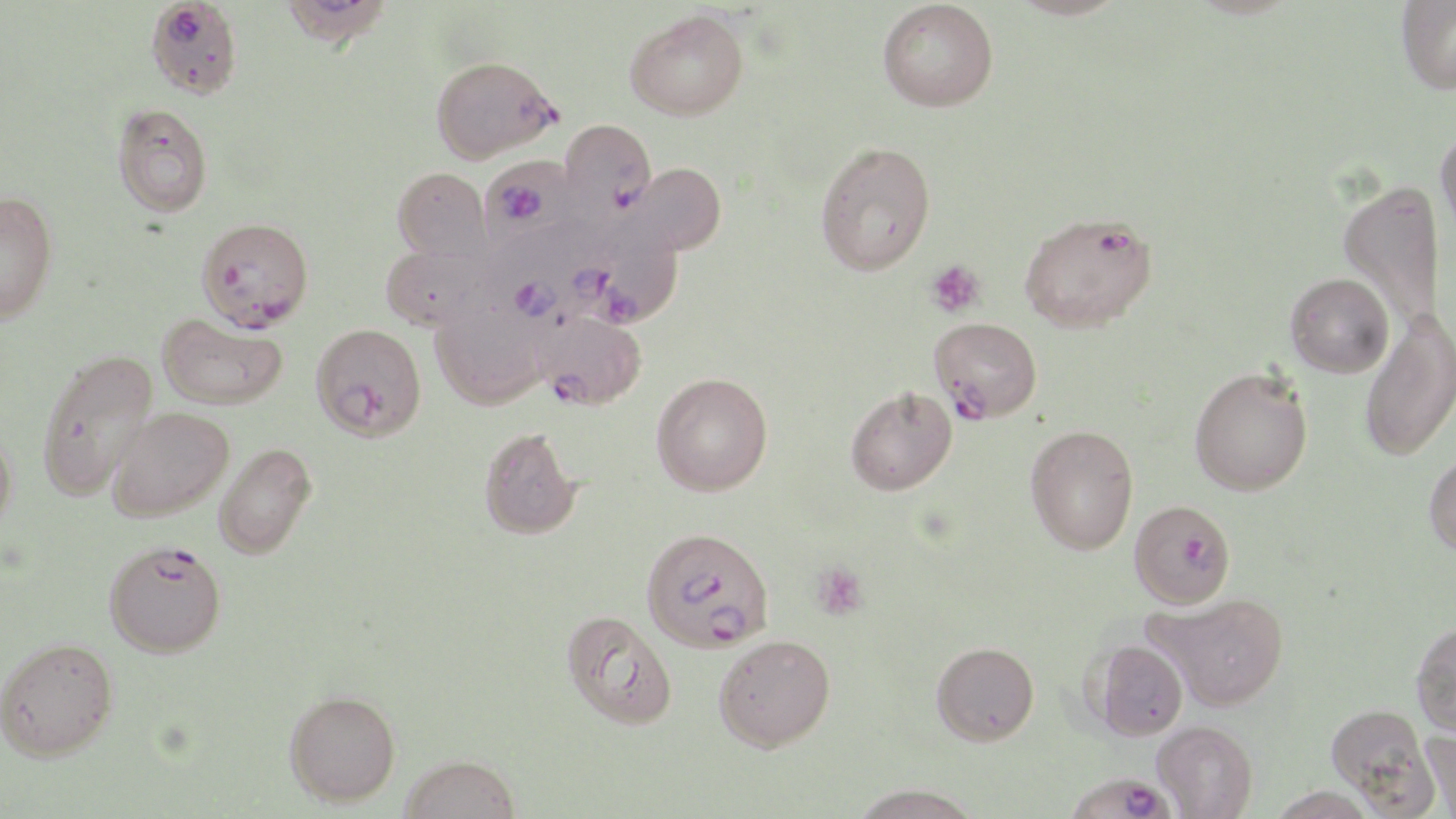

Summary:
  - Coordinate format: approximate bounding boxes as named x1/y1/x2/y2 corners in pixels
  - Plasmodium falciparum-infected red blood cell locations (subset): (x1=278, y1=0, x2=392, y2=49), (x1=430, y1=55, x2=560, y2=163), (x1=559, y1=118, x2=657, y2=221), (x1=479, y1=156, x2=584, y2=243), (x1=1019, y1=210, x2=1158, y2=333), (x1=196, y1=216, x2=313, y2=330), (x1=580, y1=216, x2=684, y2=328), (x1=485, y1=231, x2=602, y2=340), (x1=535, y1=310, x2=647, y2=410), (x1=929, y1=316, x2=1042, y2=422), (x1=311, y1=322, x2=427, y2=441), (x1=1129, y1=500, x2=1235, y2=608), (x1=641, y1=527, x2=775, y2=653), (x1=104, y1=539, x2=226, y2=657), (x1=1063, y1=772, x2=1177, y2=818)
  - Uninfected red blood cell locations (subset): (x1=878, y1=0, x2=998, y2=112), (x1=1009, y1=0, x2=1128, y2=20), (x1=1396, y1=0, x2=1456, y2=94), (x1=625, y1=8, x2=748, y2=120), (x1=113, y1=104, x2=213, y2=217), (x1=1435, y1=125, x2=1456, y2=247), (x1=815, y1=140, x2=935, y2=275), (x1=626, y1=162, x2=726, y2=255), (x1=392, y1=167, x2=491, y2=261), (x1=1339, y1=180, x2=1445, y2=326), (x1=0, y1=191, x2=58, y2=323), (x1=381, y1=244, x2=494, y2=331), (x1=1285, y1=272, x2=1394, y2=377), (x1=430, y1=297, x2=549, y2=410), (x1=1360, y1=309, x2=1456, y2=462), (x1=156, y1=312, x2=288, y2=409), (x1=36, y1=348, x2=159, y2=500), (x1=1189, y1=367, x2=1313, y2=496), (x1=651, y1=372, x2=773, y2=496), (x1=845, y1=386, x2=957, y2=496), (x1=107, y1=406, x2=234, y2=521), (x1=1025, y1=424, x2=1138, y2=554), (x1=479, y1=426, x2=582, y2=539), (x1=0, y1=429, x2=17, y2=536), (x1=214, y1=442, x2=317, y2=559), (x1=1424, y1=449, x2=1456, y2=558), (x1=1146, y1=593, x2=1290, y2=710), (x1=561, y1=610, x2=678, y2=731), (x1=1410, y1=620, x2=1456, y2=736), (x1=714, y1=634, x2=835, y2=751), (x1=0, y1=636, x2=118, y2=761), (x1=1091, y1=640, x2=1188, y2=740), (x1=931, y1=641, x2=1039, y2=745), (x1=284, y1=689, x2=401, y2=806), (x1=1325, y1=704, x2=1436, y2=814), (x1=1153, y1=721, x2=1257, y2=819), (x1=1420, y1=725, x2=1456, y2=817), (x1=399, y1=754, x2=521, y2=818), (x1=850, y1=783, x2=982, y2=818)
  - Platelet locations: (x1=925, y1=260, x2=985, y2=318), (x1=811, y1=561, x2=868, y2=620)
  - Slide-level diagnosis: Plasmodium falciparum
  - Preparation: thin blood film
  - Modality: light microscopy
  - Image size: 1456×819 pixels
  - Magnification: 1000x
  - Stain: May-Grünwald-Giemsa
  - Field of view: one of a larger specimen